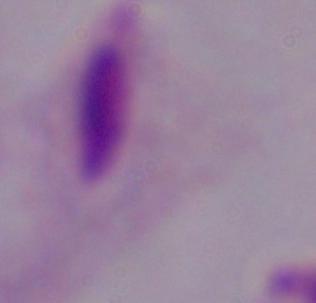

{
  "magnification": "1000x",
  "identification": "trichomonad",
  "modality": "micrograph"
}